Give the extent of all Plasmodium ovale-infected red blood cells.
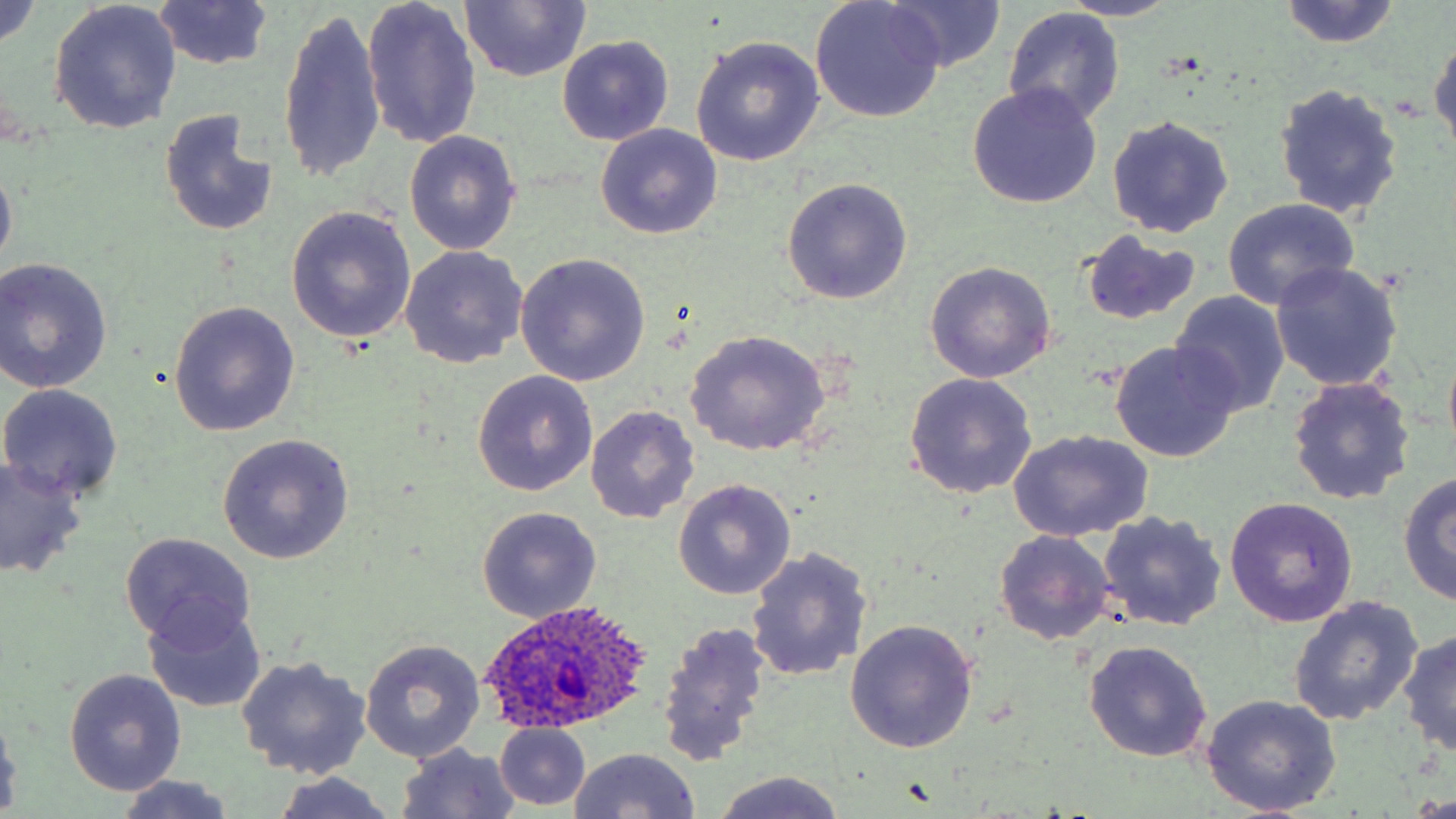
Approximate bounding boxes as (x1, y1, x2, y2) in pixels.
Plasmodium ovale-infected red blood cells: (480, 603, 657, 735).

Uninfected red blood cell locations: (362, 0, 482, 150), (877, 0, 1008, 74), (0, 1, 43, 52), (1058, 1, 1184, 22), (1279, 1, 1401, 48), (459, 2, 590, 83), (810, 2, 946, 122), (49, 3, 182, 135), (151, 3, 276, 71), (276, 6, 385, 187), (1003, 8, 1126, 126), (1429, 30, 1456, 156), (557, 35, 674, 146), (689, 37, 825, 168), (1274, 83, 1404, 220), (967, 85, 1101, 208), (160, 109, 279, 240), (1107, 116, 1234, 237), (596, 124, 722, 239), (404, 130, 522, 256), (0, 157, 17, 277), (780, 177, 913, 303), (1221, 198, 1361, 310), (287, 206, 419, 344), (1079, 231, 1202, 326), (399, 245, 528, 368), (515, 254, 653, 386), (0, 258, 113, 393), (1270, 262, 1403, 393), (924, 263, 1056, 384), (1170, 292, 1290, 417), (168, 301, 301, 436), (682, 331, 831, 457), (1109, 341, 1239, 464), (1442, 345, 1456, 458), (472, 371, 597, 496), (903, 373, 1037, 499), (1287, 377, 1415, 506), (0, 384, 124, 503), (585, 405, 699, 523), (1008, 430, 1153, 542), (218, 433, 354, 564), (0, 456, 89, 579), (1049, 456, 1194, 598), (1396, 472, 1456, 606), (673, 481, 796, 601), (1224, 497, 1357, 628), (476, 508, 602, 623), (1098, 510, 1227, 632), (994, 530, 1116, 646), (119, 532, 255, 648), (747, 547, 871, 683), (1288, 597, 1423, 727), (144, 602, 268, 713), (656, 620, 771, 767), (845, 620, 979, 754), (1397, 629, 1456, 757), (360, 638, 486, 763), (1083, 640, 1212, 762), (235, 656, 372, 779), (65, 669, 187, 795), (1200, 694, 1341, 815), (0, 707, 23, 814), (495, 724, 590, 810), (396, 744, 522, 819), (568, 748, 702, 819), (711, 771, 846, 819), (270, 772, 398, 819), (113, 776, 242, 817). Slide-level diagnosis: Plasmodium ovale. Thin blood film. One field of a larger specimen. Captured at 1000x magnification. Image is 1456×819 pixels. Light microscopy. May-Grünwald-Giemsa-stained preparation.